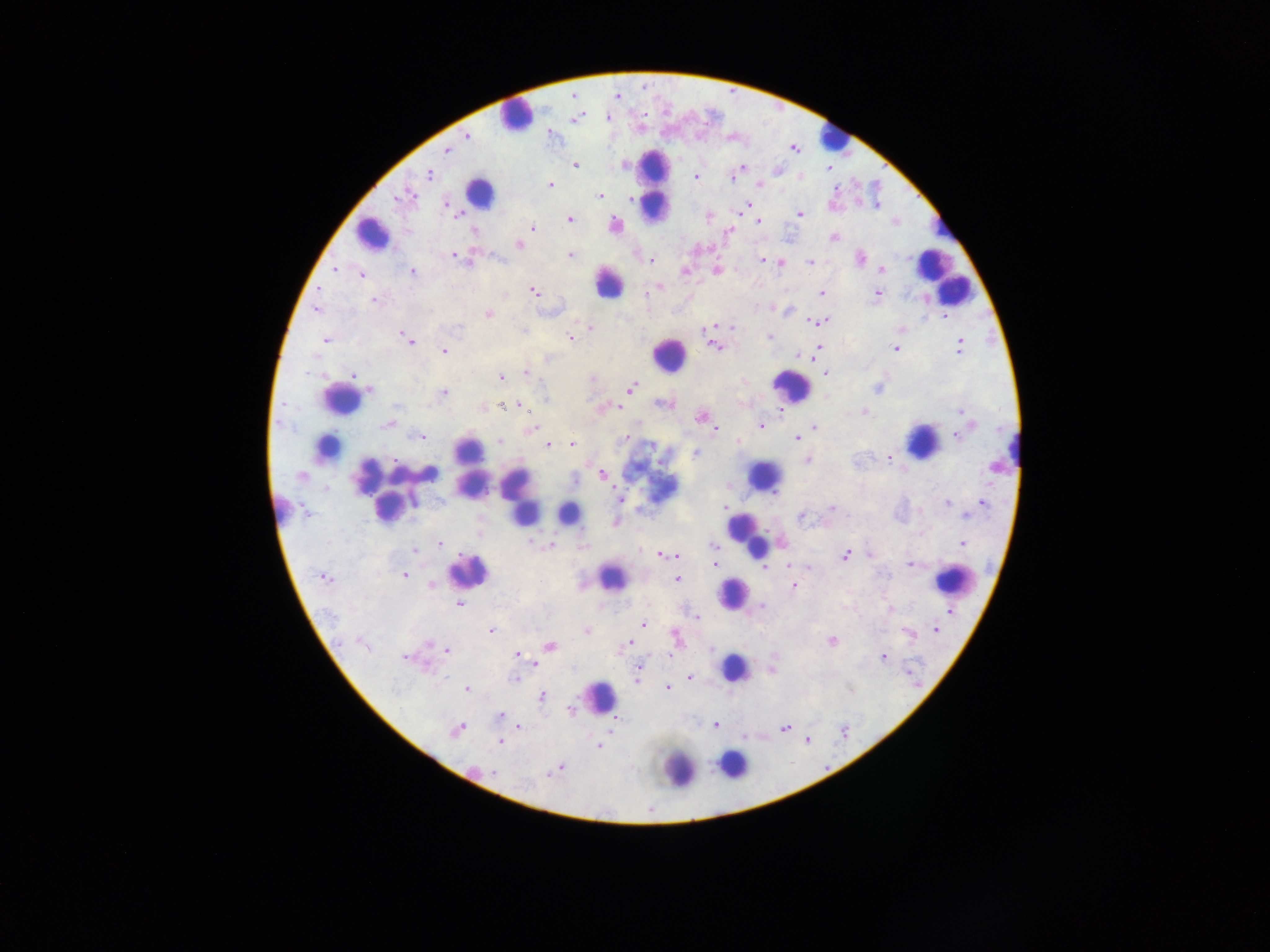
Approximate centers as x y in pixels. Malaria parasite locations: 617 96; 467 136; 446 150; 575 165; 742 167; 829 169; 429 174; 696 177; 733 177; 550 184; 759 184; 411 196; 600 196; 398 198; 632 198; 445 204; 748 205; 877 205; 800 213; 458 216; 709 217; 569 219; 758 221; 893 222; 615 225; 533 228; 473 230; 729 232; 833 237; 519 244; 454 255; 570 255; 459 258; 762 259; 860 259; 651 260; 810 262; 781 263; 335 269; 881 269; 717 270; 685 271; 412 272; 362 275; 659 287; 534 292; 822 293; 877 294; 374 300; 316 309; 790 311; 488 314; 945 316; 823 321; 813 322; 732 326; 460 327; 590 328; 901 329; 769 336; 405 338; 570 338; 324 339; 409 341; 959 346; 714 347; 821 347; 894 348; 444 351; 798 355; 810 357; 547 358; 526 372; 353 374; 825 374; 502 377; 591 379; 632 388; 877 388; 370 390; 444 392; 545 397; 663 404; 395 406; 501 406; 521 407; 618 407; 864 411; 960 412; 700 418; 386 425; 760 426; 532 428; 816 428; 715 429; 958 435; 420 437; 625 438; 796 438; 497 441; 739 442; 572 444; 547 446; 696 453; 888 457; 807 461; 994 467; 603 474; 302 476; 575 479; 620 498; 414 501; 946 502; 983 503; 724 507; 832 508; 305 512; 967 514; 802 517; 615 522; 531 542; 441 543; 962 544; 552 545; 713 545; 414 550; 870 554; 664 555; 845 555; 716 564; 790 564; 910 564; 767 567; 808 568; 405 576; 324 577; 677 579; 430 586; 793 586; 458 604; 761 606; 891 608; 951 612; 697 617; 643 624; 936 629; 587 631; 491 632; 908 634; 675 637; 831 642; 630 643; 363 645; 429 645; 550 646; 711 649; 447 651; 517 654; 670 655; 405 657; 883 657; 536 663; 639 669; 690 678; 515 680; 668 687; 467 688; 542 696; 569 710; 500 715; 615 720; 715 725; 520 727; 785 728; 456 730; 807 740; 501 741; 599 746; 559 768; 556 770; 494 772; 550 774. Object labeled both malaria parasite and leukocyte by the source: 567 514. Leukocyte locations (subset; some below the resolvable size): 515 113; 832 137; 654 185; 479 193; 943 229; 373 235; 942 274; 610 282; 669 354; 791 387; 340 399; 923 442; 330 446; 467 449; 1017 450; 397 471; 370 475; 766 475; 425 477; 471 486; 519 495; 387 507; 281 508; 745 533; 752 544; 468 569; 611 578; 954 580; 734 593; 735 668; 599 695; 734 766; 680 768. One field of view. Image is 1270×952 pixels. Photographed through a microscope with a mobile-phone camera. Thick blood smear. Collected in Ghana.